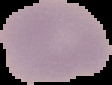
image_type: segmented cell region with the area outside set to black
preparation: thin blood smear
image_size: 112×85 pixels
malaria_status: uninfected